Locate and identify every blood parasite.
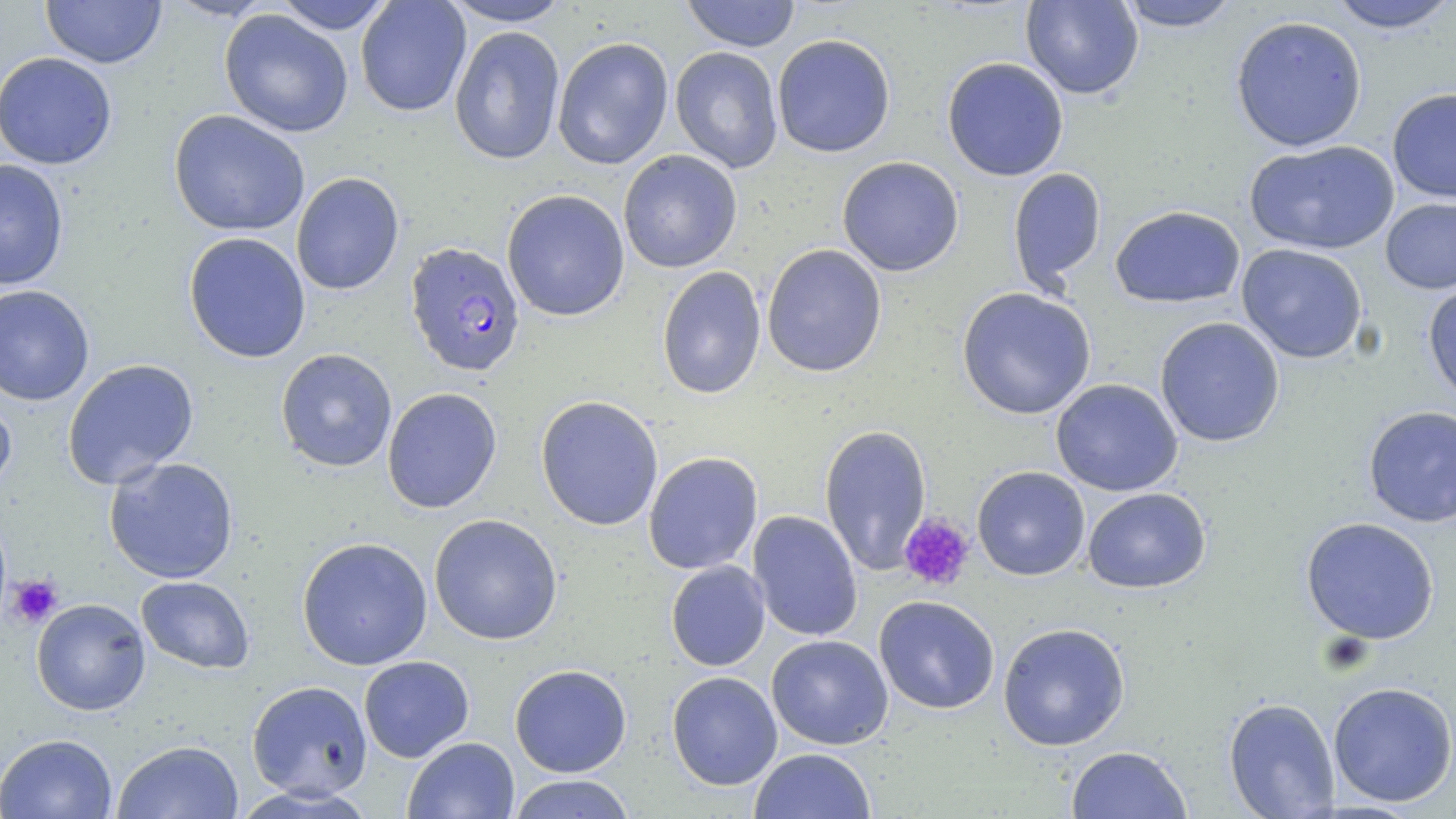
Approximate bounding boxes as named x1/y1/x2/y2 corners in pixels.
Plasmodium falciparum-infected red blood cells: (x1=405, y1=241, x2=526, y2=377).
No Plasmodium ovale, Plasmodium malariae, Plasmodium vivax, Babesia divergens, or Trypanosoma brucei observed.

Platelet locations: (x1=899, y1=513, x2=975, y2=590), (x1=5, y1=574, x2=63, y2=627). Uninfected red blood cell locations: (x1=41, y1=0, x2=166, y2=68), (x1=356, y1=0, x2=471, y2=117), (x1=440, y1=0, x2=573, y2=26), (x1=680, y1=0, x2=801, y2=52), (x1=1020, y1=0, x2=1144, y2=100), (x1=1325, y1=0, x2=1455, y2=33), (x1=273, y1=1, x2=395, y2=34), (x1=1114, y1=1, x2=1242, y2=32), (x1=219, y1=9, x2=354, y2=138), (x1=1230, y1=15, x2=1368, y2=152), (x1=449, y1=26, x2=565, y2=166), (x1=772, y1=33, x2=896, y2=158), (x1=552, y1=36, x2=674, y2=170), (x1=670, y1=46, x2=783, y2=173), (x1=0, y1=51, x2=117, y2=169), (x1=942, y1=57, x2=1069, y2=181), (x1=1387, y1=88, x2=1456, y2=203), (x1=168, y1=109, x2=310, y2=237), (x1=1245, y1=140, x2=1399, y2=255), (x1=618, y1=150, x2=742, y2=273), (x1=837, y1=156, x2=964, y2=276), (x1=0, y1=158, x2=69, y2=290), (x1=1008, y1=168, x2=1107, y2=295), (x1=291, y1=172, x2=405, y2=296), (x1=501, y1=189, x2=630, y2=321), (x1=1380, y1=197, x2=1456, y2=295), (x1=1110, y1=205, x2=1246, y2=308), (x1=183, y1=232, x2=311, y2=363), (x1=761, y1=244, x2=887, y2=377), (x1=1236, y1=244, x2=1368, y2=364), (x1=656, y1=266, x2=767, y2=399), (x1=1422, y1=280, x2=1456, y2=406), (x1=0, y1=284, x2=95, y2=406), (x1=957, y1=287, x2=1096, y2=420), (x1=1154, y1=317, x2=1285, y2=447), (x1=276, y1=348, x2=397, y2=472), (x1=62, y1=358, x2=199, y2=490), (x1=1050, y1=378, x2=1183, y2=496), (x1=382, y1=386, x2=502, y2=514), (x1=0, y1=389, x2=17, y2=500), (x1=535, y1=395, x2=664, y2=530), (x1=1363, y1=405, x2=1456, y2=528), (x1=819, y1=424, x2=932, y2=576), (x1=644, y1=451, x2=763, y2=575), (x1=104, y1=456, x2=239, y2=584), (x1=972, y1=466, x2=1090, y2=580), (x1=1083, y1=487, x2=1211, y2=594), (x1=748, y1=510, x2=863, y2=642), (x1=428, y1=513, x2=563, y2=645), (x1=1300, y1=516, x2=1440, y2=645), (x1=296, y1=536, x2=433, y2=671), (x1=666, y1=560, x2=770, y2=671), (x1=136, y1=576, x2=255, y2=674), (x1=874, y1=595, x2=1000, y2=715), (x1=31, y1=598, x2=150, y2=715), (x1=998, y1=622, x2=1130, y2=750), (x1=766, y1=634, x2=894, y2=750), (x1=358, y1=655, x2=474, y2=763), (x1=509, y1=663, x2=632, y2=777), (x1=666, y1=670, x2=782, y2=790), (x1=246, y1=680, x2=373, y2=800), (x1=1327, y1=681, x2=1456, y2=807), (x1=1223, y1=697, x2=1340, y2=818), (x1=1, y1=733, x2=117, y2=819), (x1=403, y1=737, x2=520, y2=819), (x1=112, y1=740, x2=245, y2=819), (x1=1065, y1=745, x2=1192, y2=818), (x1=750, y1=748, x2=876, y2=819), (x1=506, y1=774, x2=636, y2=818). Slide-level diagnosis: Plasmodium falciparum. Optical microscopy. Thin blood smear. Single field of view. Captured at 1000x magnification. Image is 1456×819 pixels. May-Grünwald-Giemsa-stained preparation.